Classify this cell by malaria status.
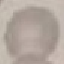

It is uninfected.

{
  "stain": "Giemsa",
  "preparation": "thin blood film",
  "capture": "smartphone camera at the microscope eyepiece",
  "image_type": "automatically extracted cell patch, resized to 64 × 64 pixels"
}